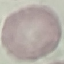
result: negative for malaria parasites
capture: smartphone camera at the microscope eyepiece
preparation: thin smear
stain: Giemsa
image_type: automatically extracted cell patch, resized to 64 × 64 pixels